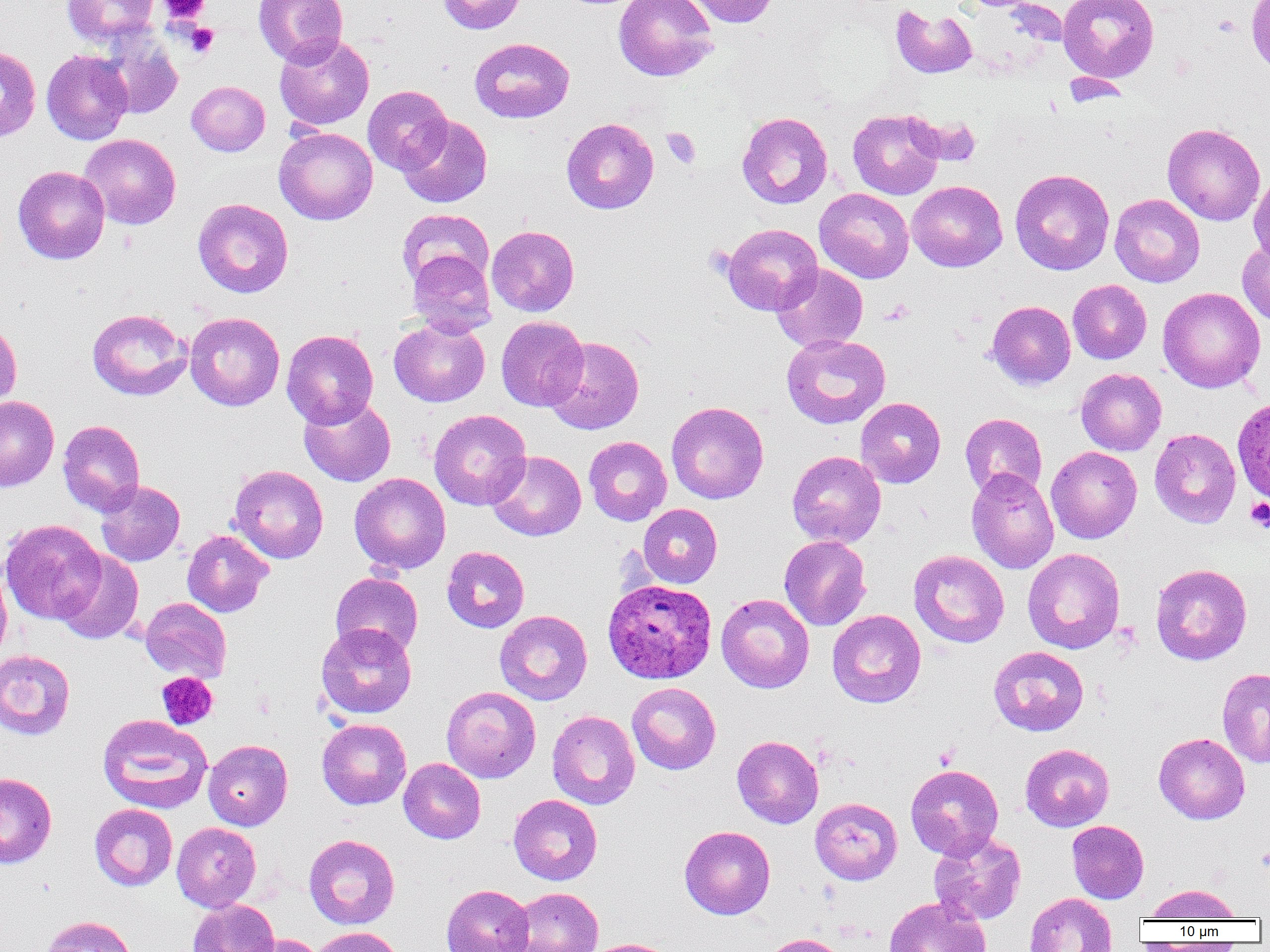

Approximate bounding boxes as named x1/y1/x2/y2 corners in pixels. Uninfected red blood cell locations: (x1=62, y1=0, x2=160, y2=46), (x1=254, y1=0, x2=348, y2=67), (x1=438, y1=0, x2=526, y2=34), (x1=614, y1=0, x2=718, y2=82), (x1=684, y1=0, x2=778, y2=28), (x1=1058, y1=0, x2=1159, y2=82), (x1=1246, y1=0, x2=1270, y2=77), (x1=890, y1=4, x2=978, y2=79), (x1=96, y1=29, x2=183, y2=120), (x1=274, y1=35, x2=374, y2=130), (x1=469, y1=37, x2=575, y2=123), (x1=0, y1=46, x2=41, y2=142), (x1=41, y1=50, x2=133, y2=145), (x1=186, y1=81, x2=270, y2=156), (x1=363, y1=85, x2=452, y2=174), (x1=848, y1=108, x2=945, y2=199), (x1=736, y1=111, x2=833, y2=209), (x1=907, y1=113, x2=984, y2=167), (x1=398, y1=115, x2=492, y2=208), (x1=561, y1=117, x2=659, y2=214), (x1=1163, y1=123, x2=1265, y2=225), (x1=274, y1=126, x2=377, y2=224), (x1=79, y1=134, x2=181, y2=229), (x1=13, y1=165, x2=110, y2=264), (x1=1010, y1=168, x2=1114, y2=275), (x1=1248, y1=172, x2=1270, y2=266), (x1=907, y1=180, x2=1007, y2=272), (x1=814, y1=188, x2=914, y2=283), (x1=1109, y1=194, x2=1205, y2=287), (x1=193, y1=198, x2=294, y2=298), (x1=397, y1=208, x2=494, y2=291), (x1=721, y1=223, x2=822, y2=315), (x1=487, y1=225, x2=579, y2=316), (x1=1237, y1=240, x2=1270, y2=326), (x1=408, y1=250, x2=496, y2=337), (x1=771, y1=263, x2=868, y2=352), (x1=1068, y1=279, x2=1151, y2=364), (x1=1158, y1=287, x2=1265, y2=393), (x1=987, y1=301, x2=1075, y2=389), (x1=87, y1=308, x2=191, y2=400), (x1=185, y1=312, x2=285, y2=410), (x1=496, y1=316, x2=589, y2=411), (x1=389, y1=318, x2=490, y2=407), (x1=0, y1=319, x2=22, y2=412), (x1=282, y1=329, x2=378, y2=427), (x1=781, y1=333, x2=891, y2=429), (x1=544, y1=336, x2=644, y2=434), (x1=1075, y1=368, x2=1166, y2=456), (x1=299, y1=394, x2=396, y2=486), (x1=0, y1=395, x2=59, y2=491), (x1=856, y1=398, x2=946, y2=488), (x1=666, y1=401, x2=769, y2=504), (x1=428, y1=409, x2=531, y2=510), (x1=960, y1=413, x2=1047, y2=499), (x1=58, y1=420, x2=146, y2=516), (x1=1149, y1=428, x2=1241, y2=528), (x1=584, y1=436, x2=672, y2=525), (x1=1046, y1=446, x2=1142, y2=543), (x1=487, y1=450, x2=586, y2=541), (x1=787, y1=450, x2=886, y2=547), (x1=229, y1=464, x2=328, y2=563), (x1=966, y1=468, x2=1059, y2=574), (x1=349, y1=473, x2=450, y2=574), (x1=95, y1=481, x2=185, y2=566), (x1=638, y1=504, x2=722, y2=588), (x1=0, y1=519, x2=107, y2=624), (x1=182, y1=530, x2=273, y2=617), (x1=779, y1=535, x2=871, y2=631), (x1=442, y1=546, x2=529, y2=633), (x1=1023, y1=548, x2=1125, y2=654), (x1=909, y1=549, x2=1009, y2=648), (x1=55, y1=550, x2=144, y2=644), (x1=1150, y1=563, x2=1252, y2=665), (x1=0, y1=564, x2=12, y2=665), (x1=331, y1=572, x2=423, y2=658), (x1=716, y1=594, x2=815, y2=693), (x1=140, y1=597, x2=232, y2=683), (x1=827, y1=609, x2=926, y2=708), (x1=495, y1=610, x2=592, y2=705), (x1=316, y1=622, x2=416, y2=719), (x1=989, y1=646, x2=1089, y2=736), (x1=0, y1=650, x2=75, y2=740), (x1=1217, y1=668, x2=1270, y2=767), (x1=627, y1=682, x2=721, y2=774), (x1=441, y1=686, x2=541, y2=783), (x1=547, y1=710, x2=640, y2=809), (x1=97, y1=714, x2=212, y2=813), (x1=317, y1=719, x2=411, y2=809), (x1=1154, y1=732, x2=1249, y2=824), (x1=732, y1=735, x2=824, y2=828), (x1=203, y1=739, x2=292, y2=830), (x1=1020, y1=743, x2=1114, y2=832), (x1=398, y1=758, x2=486, y2=844), (x1=905, y1=764, x2=1004, y2=859), (x1=0, y1=772, x2=56, y2=869), (x1=508, y1=794, x2=602, y2=885), (x1=810, y1=797, x2=903, y2=884), (x1=89, y1=803, x2=177, y2=891), (x1=1067, y1=820, x2=1149, y2=903), (x1=172, y1=822, x2=261, y2=912), (x1=679, y1=825, x2=775, y2=919), (x1=928, y1=831, x2=1026, y2=925), (x1=304, y1=834, x2=400, y2=929), (x1=441, y1=884, x2=534, y2=952), (x1=1145, y1=884, x2=1242, y2=921), (x1=507, y1=887, x2=604, y2=952), (x1=1024, y1=892, x2=1117, y2=952), (x1=884, y1=896, x2=991, y2=952), (x1=187, y1=898, x2=280, y2=952), (x1=39, y1=915, x2=138, y2=952), (x1=309, y1=926, x2=404, y2=952), (x1=762, y1=933, x2=849, y2=952), (x1=237, y1=934, x2=328, y2=952), (x1=584, y1=938, x2=680, y2=952). Platelet locations: (x1=159, y1=0, x2=211, y2=23), (x1=185, y1=23, x2=218, y2=57), (x1=661, y1=127, x2=701, y2=169), (x1=882, y1=299, x2=914, y2=325), (x1=1246, y1=498, x2=1270, y2=531), (x1=156, y1=672, x2=218, y2=730). Plasmodium ovale-infected red blood cell locations: (x1=1233, y1=396, x2=1270, y2=505), (x1=602, y1=578, x2=717, y2=684). Slide-level diagnosis: Plasmodium ovale. Captured at 1000x magnification. Image is 1270×952 pixels. Thin blood smear. One field of a larger specimen. Light microscopy.